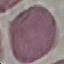

result = negative for malaria parasites
stain = Giemsa
capture = smartphone camera at the microscope eyepiece
image type = cell patch, automatically extracted from a larger field of view and resized to 64 × 64 pixels
preparation = thin blood film